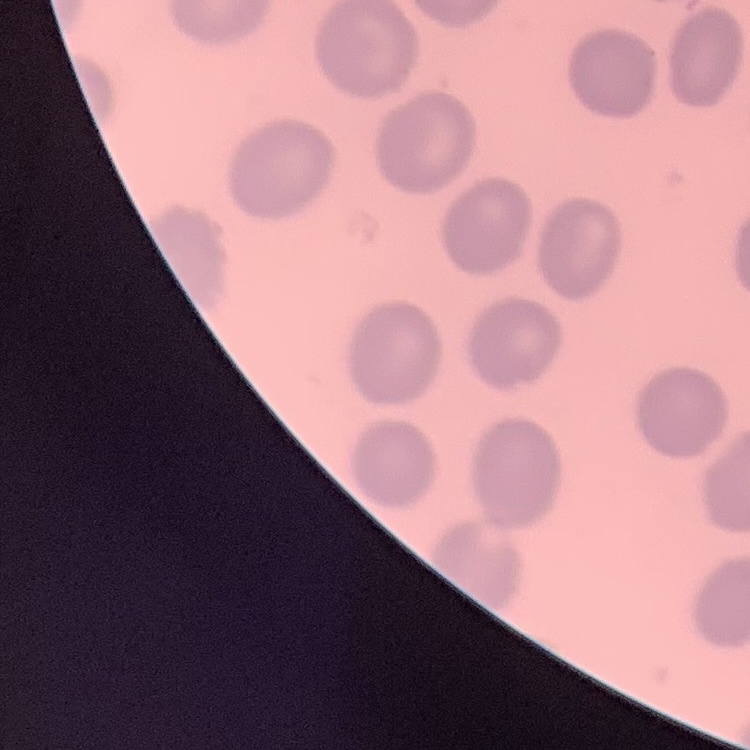
Summary:
  - Red blood cell morphology: no rouleaux formation
  - Image type: one tile cut from a larger photomicrograph
  - Stain: Field's or Giemsa
  - Preparation: thin peripheral smear